Locate every blood parasite and identify its species.
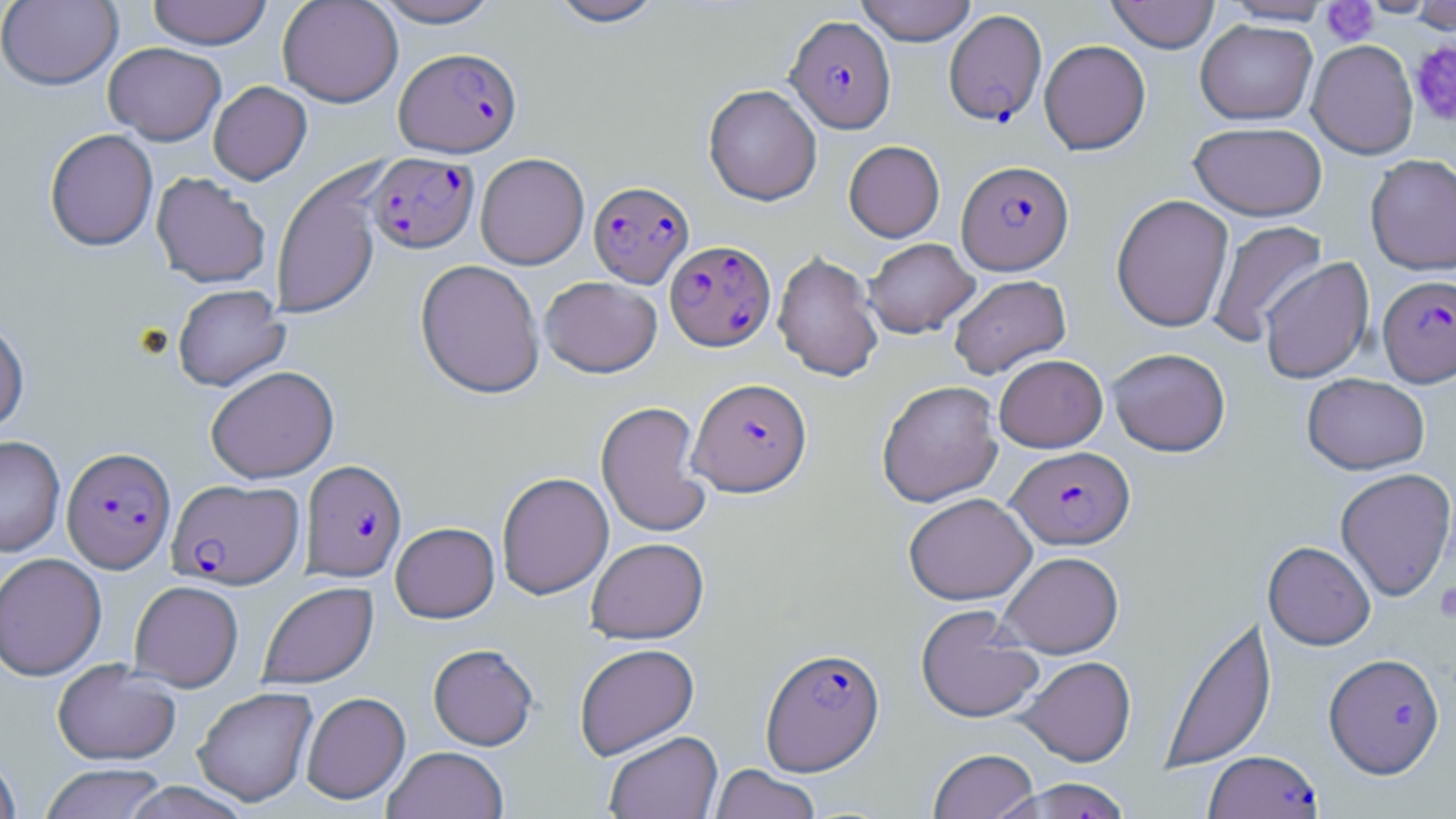

Approximate bounding boxes as (x1,y1)-(x2,y2) corner pairs in pixels.
Plasmodium falciparum-infected red blood cells: (944,9)-(1047,127), (786,15)-(896,133), (395,47)-(522,158), (368,152)-(479,253), (957,160)-(1073,274), (588,180)-(694,288), (665,240)-(776,351), (1378,274)-(1456,387), (688,377)-(812,497), (62,446)-(176,573), (1008,446)-(1135,549), (301,460)-(407,582), (168,478)-(303,589), (761,646)-(885,776), (1324,652)-(1445,778), (1204,750)-(1323,819), (1000,776)-(1135,819).
No Plasmodium ovale, Plasmodium malariae, Plasmodium vivax, Babesia divergens, or Trypanosoma brucei observed.

slide-level diagnosis = Plasmodium falciparum
field of view = single
uninfected red blood cell locations = approximate bounding boxes as (x1,y1)-(x2,y2) corner pairs in pixels: (0,0)-(123,90), (147,0)-(272,50), (277,0)-(403,107), (370,0)-(503,28), (545,0)-(668,28), (855,0)-(977,46), (1105,0)-(1221,53), (1222,0)-(1334,25), (1410,0)-(1456,33), (1196,19)-(1317,125), (1039,39)-(1151,155), (1307,39)-(1418,159), (103,42)-(226,145), (208,81)-(312,185), (703,84)-(822,205), (1189,121)-(1327,220), (44,128)-(158,251), (844,140)-(944,242), (475,153)-(589,270), (1365,153)-(1456,274), (270,164)-(384,321), (150,172)-(271,288), (1111,194)-(1234,332), (1207,220)-(1328,346), (864,238)-(979,338), (772,250)-(884,383), (1259,257)-(1374,384), (415,259)-(545,399), (949,274)-(1071,378), (539,276)-(663,378), (172,284)-(290,391), (0,317)-(30,435), (1107,348)-(1231,456), (994,354)-(1107,452), (206,365)-(339,483), (1302,373)-(1430,475), (877,380)-(1003,506), (595,401)-(713,539), (0,435)-(65,557), (1335,467)-(1456,600), (497,472)-(614,599), (903,493)-(1036,605), (391,522)-(499,623), (586,537)-(709,644), (1263,541)-(1375,650), (998,551)-(1124,657), (0,552)-(107,681), (129,580)-(244,690), (257,581)-(378,689), (915,604)-(1043,724), (1160,613)-(1277,775), (574,643)-(700,759), (428,644)-(539,750), (1017,656)-(1136,766), (52,659)-(181,766), (192,687)-(318,806), (301,691)-(411,804), (604,731)-(723,819), (383,746)-(509,819), (928,748)-(1039,819), (0,750)-(22,819), (39,763)-(169,819), (709,765)-(821,819), (119,782)-(255,819)
platelet locations = approximate bounding boxes as (x1,y1)-(x2,y2) corner pairs in pixels: (1320,1)-(1380,46), (1409,41)-(1456,127), (1434,581)-(1456,623)
stain = May-Grünwald-Giemsa
magnification = 1000x
modality = light microscopy
preparation = thin blood smear
image size = 1456×819 pixels